Locate every Plasmodium parasite.
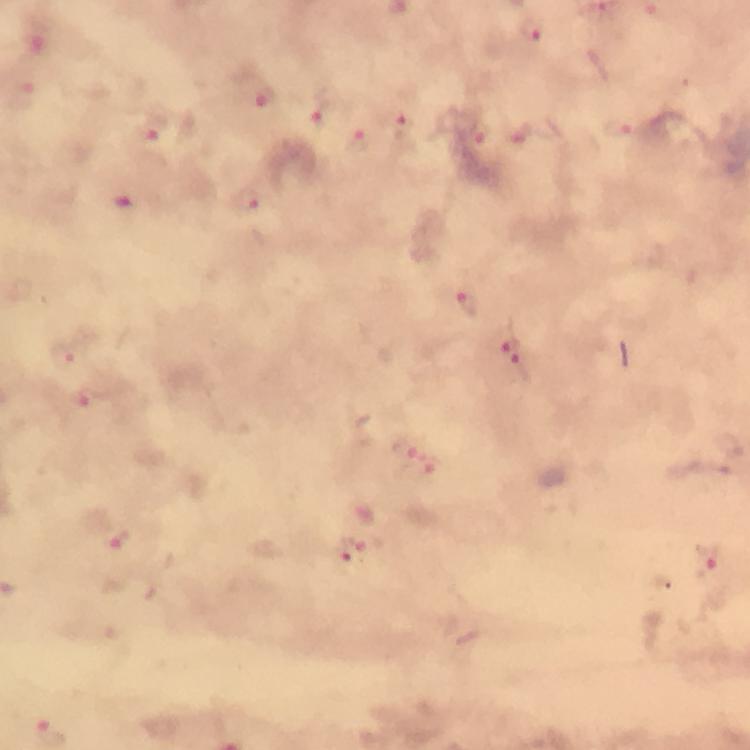
Approximate centers as (x, y) in pixels.
Plasmodium parasites: (536, 30), (23, 95), (264, 98), (319, 110), (620, 127), (405, 130), (479, 133), (154, 135), (357, 141), (245, 199), (468, 306), (510, 341), (65, 354), (523, 367), (406, 447), (119, 539), (350, 549), (707, 559).

Thick blood film. Photographed with a smartphone mounted on the microscope. Image is 750×750 pixels. Giemsa stain. Immersion oil applied. A crop from one field of view. 100x magnification. From a malaria diagnostic workup.